State which parasite is depicted.
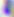

Toxoplasma gondii.

modality: micrograph
magnification: 400x